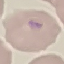 Malaria status: parasitized. Cell patch, automatically extracted from a larger field of view and resized to 64 × 64 pixels. Acquired by smartphone through the microscope eyepiece. Giemsa-stained preparation. Thin smear of blood.